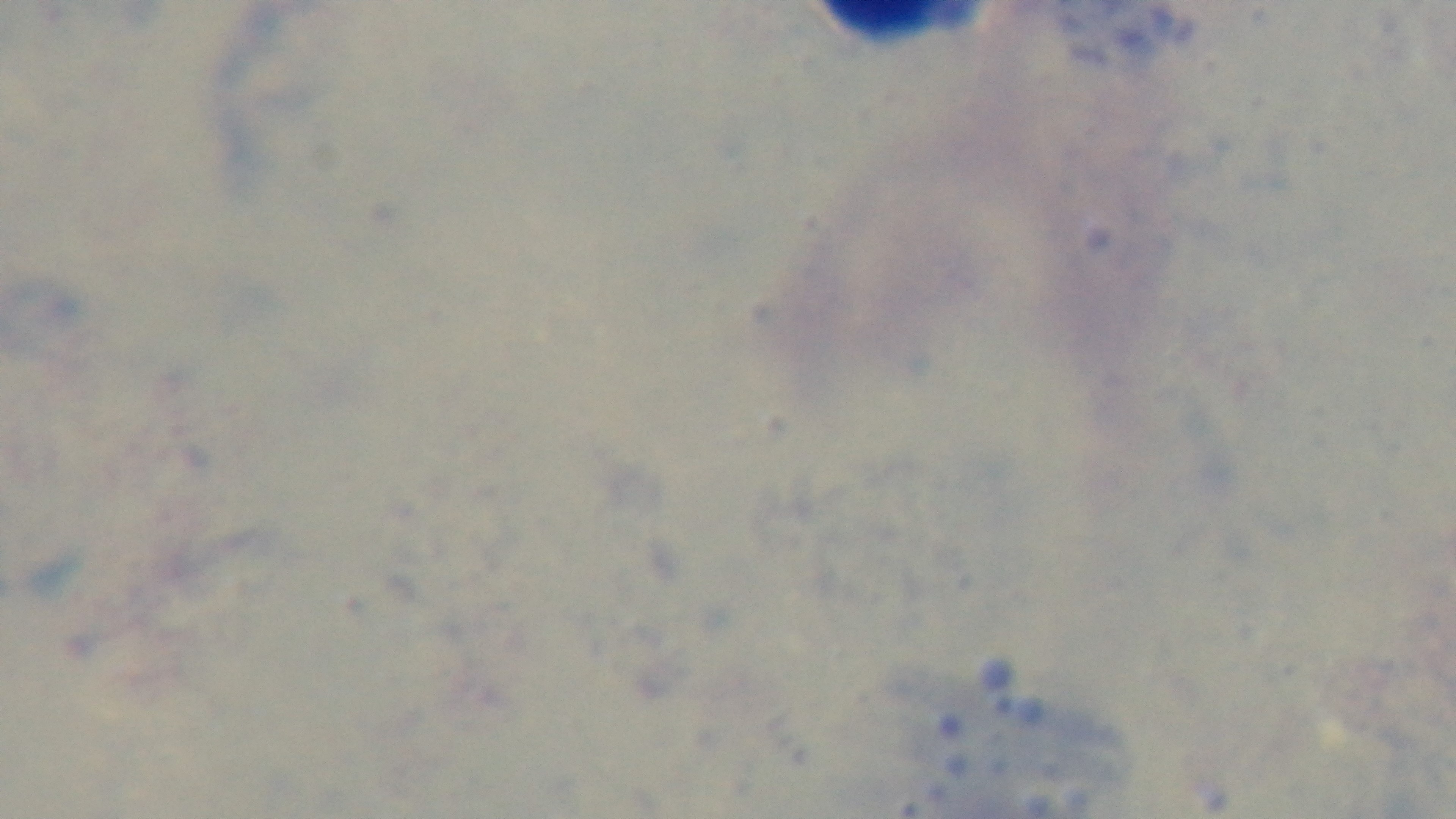

objective = 100x oil immersion
malaria status = uninfected
stain = Giemsa
field of view = one from the slide
preparation = thick
modality = light microscopy
capture = mounted 4K digital camera